Locate every Plasmodium falciparum-infected red blood cell.
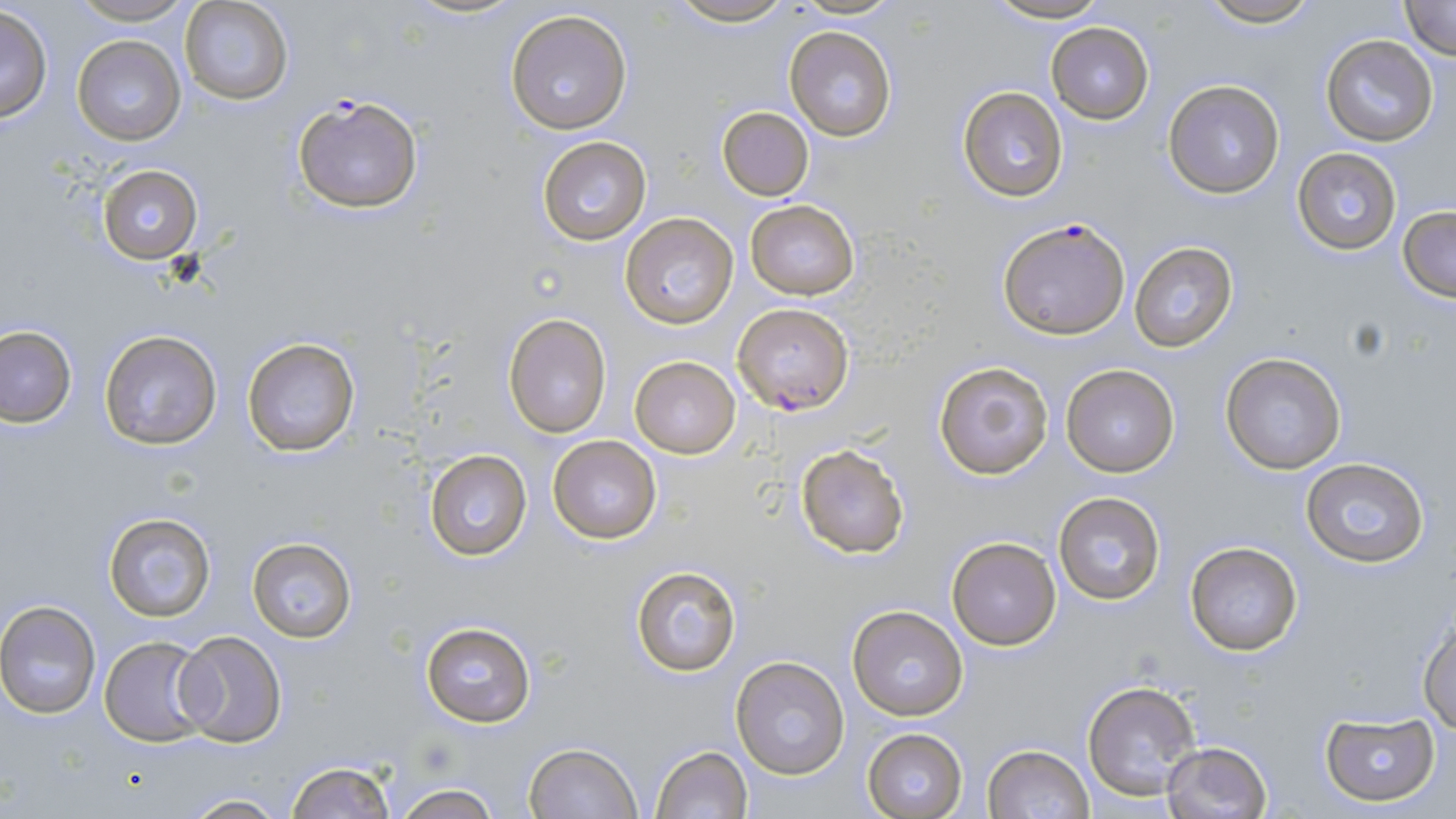
Approximate bounding boxes as (x1, y1, x2, y2) in pixels.
Plasmodium falciparum-infected red blood cells: (292, 93, 425, 215), (999, 216, 1128, 340), (733, 302, 856, 415).

Summary:
  - Uninfected red blood cell locations: (68, 0, 198, 25), (402, 0, 529, 20), (664, 0, 800, 27), (787, 0, 905, 18), (983, 0, 1115, 24), (1194, 0, 1324, 27), (180, 1, 294, 105), (1399, 1, 1456, 61), (0, 5, 52, 123), (505, 9, 633, 135), (1046, 22, 1154, 123), (784, 26, 897, 143), (1319, 33, 1439, 147), (73, 36, 186, 146), (1163, 79, 1286, 199), (956, 86, 1070, 202), (716, 105, 815, 200), (536, 136, 652, 244), (1292, 146, 1401, 257), (97, 164, 202, 265), (745, 201, 860, 300), (1397, 206, 1456, 303), (620, 212, 738, 329), (1129, 242, 1238, 351), (502, 312, 612, 439), (0, 324, 75, 427), (99, 329, 222, 450), (240, 337, 362, 458), (1220, 352, 1347, 475), (629, 355, 742, 458), (932, 358, 1054, 480), (1061, 362, 1182, 478), (548, 435, 662, 544), (795, 445, 908, 558), (424, 450, 532, 561), (1299, 456, 1431, 567), (1053, 493, 1166, 605), (102, 511, 216, 623), (947, 536, 1061, 650), (248, 538, 357, 641), (1183, 539, 1306, 658), (629, 564, 742, 677), (0, 602, 101, 718), (845, 605, 969, 721), (1417, 612, 1456, 733), (420, 620, 536, 730), (173, 631, 287, 747), (99, 636, 214, 745), (732, 655, 851, 778), (1082, 679, 1201, 801), (1320, 713, 1439, 805), (862, 728, 967, 819), (1161, 741, 1271, 819), (523, 743, 642, 819), (982, 744, 1094, 819), (649, 745, 754, 819), (285, 761, 396, 819), (387, 783, 506, 819), (179, 794, 292, 818)
  - Slide-level diagnosis: Plasmodium falciparum
  - Preparation: thin blood smear
  - Modality: optical microscopy
  - Image size: 1456×819 pixels
  - Field of view: one of a larger specimen
  - Magnification: 1000x
  - Stain: May-Grünwald-Giemsa